Outline each Plasmodium vivax-infected red blood cell.
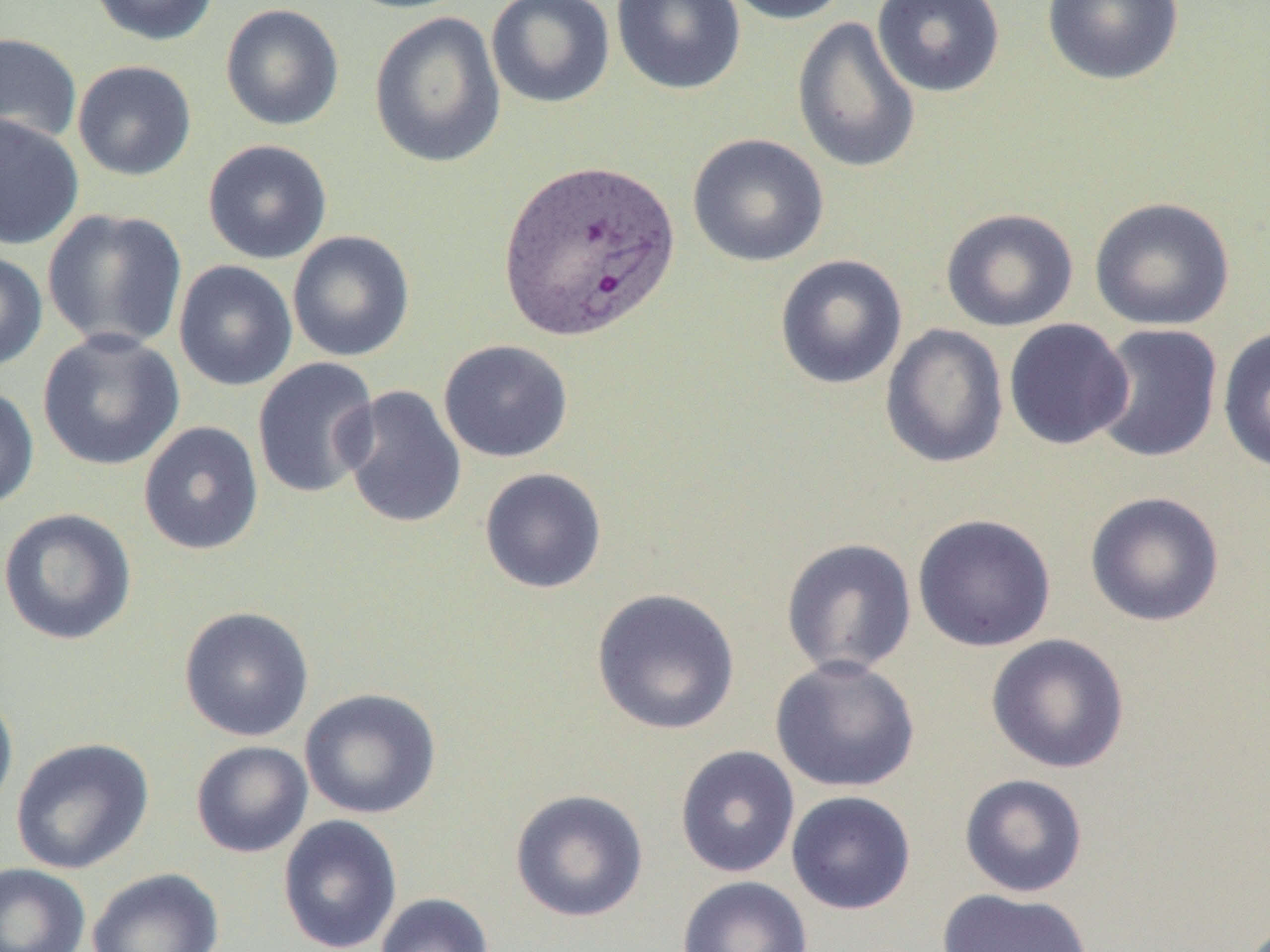
Approximate bounding boxes as named x1/y1/x2/y2 corners in pixels.
Plasmodium vivax-infected red blood cells: (x1=496, y1=158, x2=682, y2=342).

slide_level_diagnosis: Plasmodium vivax
preparation: thin blood film
magnification: 1000x
field_of_view: single
modality: optical microscopy
uninfected_red_blood_cell_locations: 'approximate bounding boxes as named x1/y1/x2/y2 corners in pixels: (x1=88, y1=0, x2=220, y2=46), (x1=337, y1=0, x2=475, y2=14), (x1=610, y1=0, x2=747, y2=95), (x1=716, y1=0, x2=852, y2=26), (x1=871, y1=0, x2=1006, y2=98), (x1=1042, y1=0, x2=1185, y2=86), (x1=485, y1=1, x2=616, y2=108), (x1=220, y1=3, x2=345, y2=131), (x1=369, y1=11, x2=506, y2=168), (x1=791, y1=16, x2=921, y2=174), (x1=0, y1=32, x2=82, y2=149), (x1=72, y1=60, x2=196, y2=181), (x1=0, y1=113, x2=84, y2=250), (x1=687, y1=133, x2=829, y2=268), (x1=202, y1=138, x2=333, y2=264), (x1=1089, y1=197, x2=1236, y2=331), (x1=940, y1=207, x2=1079, y2=332), (x1=42, y1=209, x2=188, y2=352), (x1=287, y1=230, x2=416, y2=363), (x1=0, y1=250, x2=48, y2=372), (x1=774, y1=254, x2=908, y2=390), (x1=173, y1=260, x2=298, y2=392), (x1=1003, y1=318, x2=1134, y2=450), (x1=880, y1=324, x2=1009, y2=470), (x1=1090, y1=324, x2=1223, y2=464), (x1=1217, y1=326, x2=1270, y2=474), (x1=37, y1=329, x2=185, y2=472), (x1=438, y1=339, x2=573, y2=463), (x1=252, y1=357, x2=381, y2=499), (x1=338, y1=384, x2=468, y2=530), (x1=0, y1=385, x2=40, y2=511), (x1=138, y1=421, x2=264, y2=556), (x1=479, y1=467, x2=608, y2=594), (x1=1084, y1=491, x2=1225, y2=627), (x1=0, y1=507, x2=137, y2=646), (x1=912, y1=513, x2=1057, y2=652), (x1=780, y1=537, x2=918, y2=677), (x1=591, y1=587, x2=740, y2=735), (x1=178, y1=605, x2=315, y2=742), (x1=986, y1=633, x2=1130, y2=773), (x1=770, y1=655, x2=921, y2=793), (x1=300, y1=687, x2=442, y2=819), (x1=0, y1=688, x2=19, y2=824), (x1=10, y1=737, x2=154, y2=875), (x1=190, y1=740, x2=313, y2=858), (x1=674, y1=745, x2=800, y2=878), (x1=958, y1=773, x2=1089, y2=898), (x1=509, y1=788, x2=649, y2=923), (x1=786, y1=790, x2=916, y2=915), (x1=277, y1=814, x2=402, y2=952), (x1=0, y1=863, x2=90, y2=952), (x1=86, y1=867, x2=224, y2=952), (x1=676, y1=875, x2=813, y2=952), (x1=937, y1=887, x2=1094, y2=952), (x1=374, y1=893, x2=494, y2=952)'
image_size: 1270×952 pixels